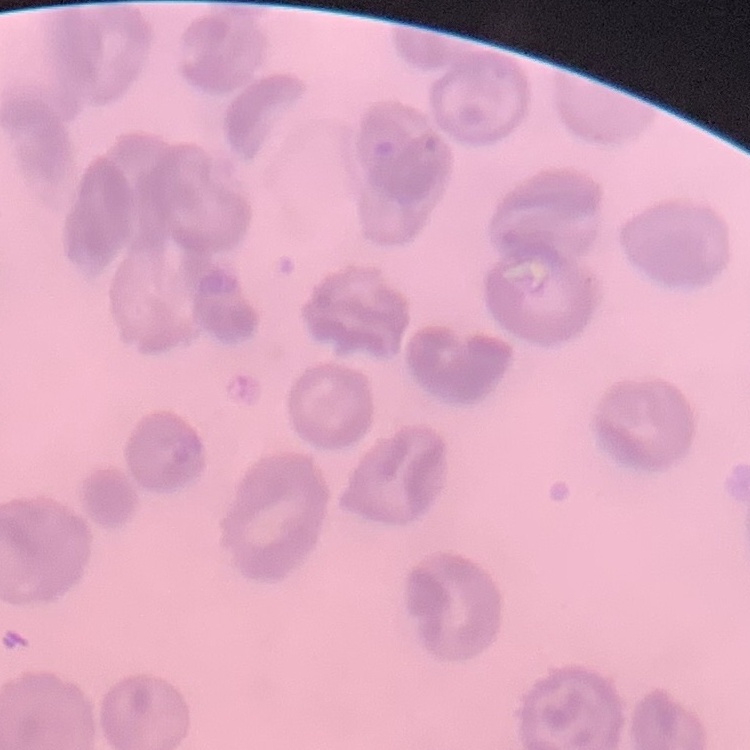

The erythrocytes exhibit no rouleaux formation. One tile cut from a larger photomicrograph. Stained with either Field's or Giemsa. Thin blood film.